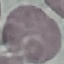

result: negative for malaria parasites
preparation: thin smear
stain: Giemsa
capture: smartphone through the microscope eyepiece
image_type: automatically extracted cell patch, resized to 64 × 64 pixels